Comment on the morphology of the erythrocytes.
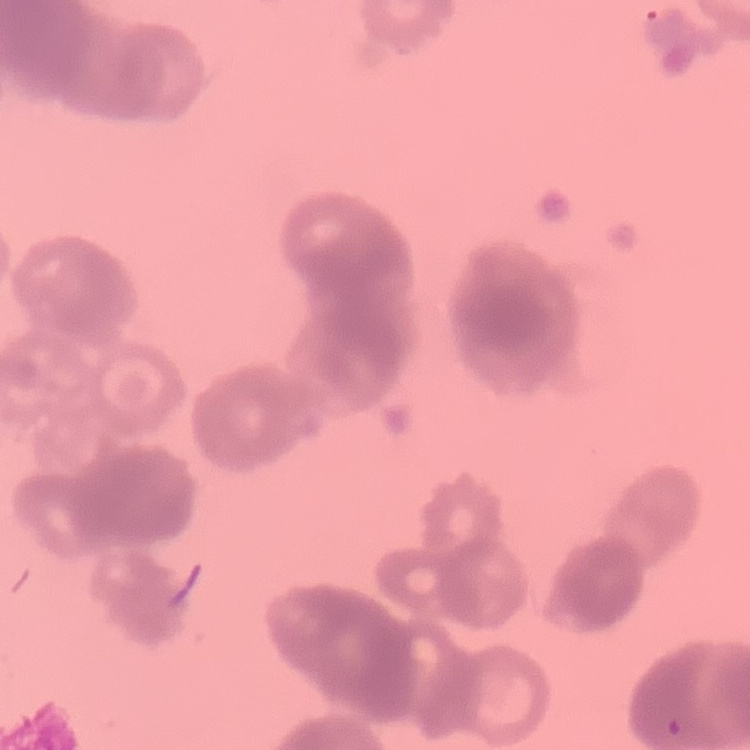
They show rouleaux formation.

stain = Field's or Giemsa
image type = square crop of a larger photomicrograph
preparation = thin blood film